Comment on the morphology of the red blood cells.
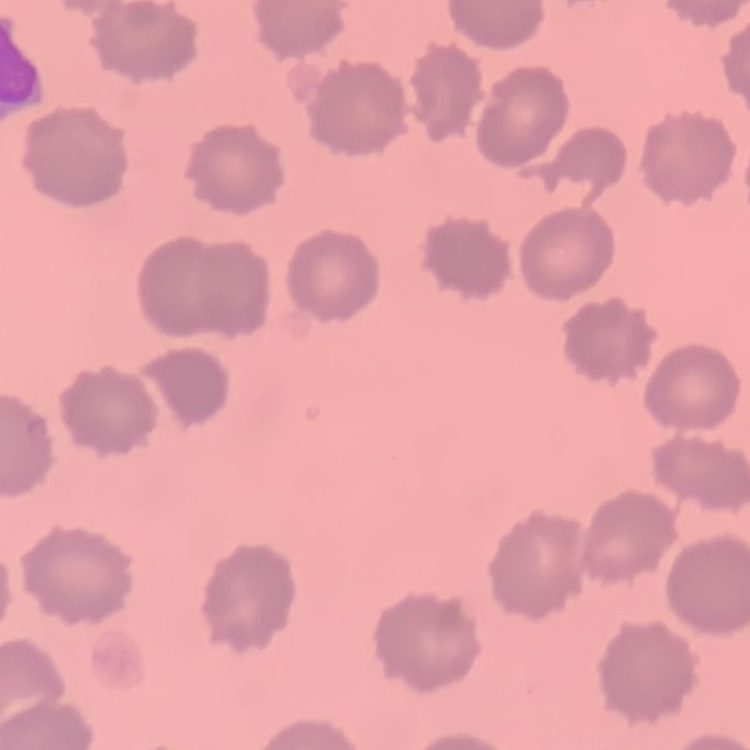

They show no rouleaux formation.

Field's or Giemsa stain. Thin blood smear. Square crop of a larger photomicrograph.